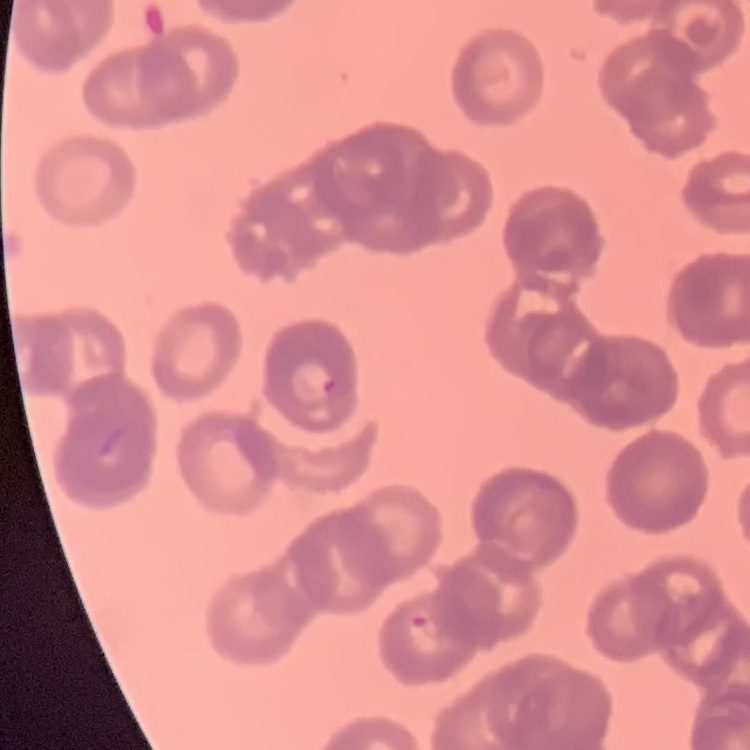 The red blood cells show rouleaux formation. One tile cut from a larger photomicrograph. Field's or Giemsa stain. Thin peripheral smear.